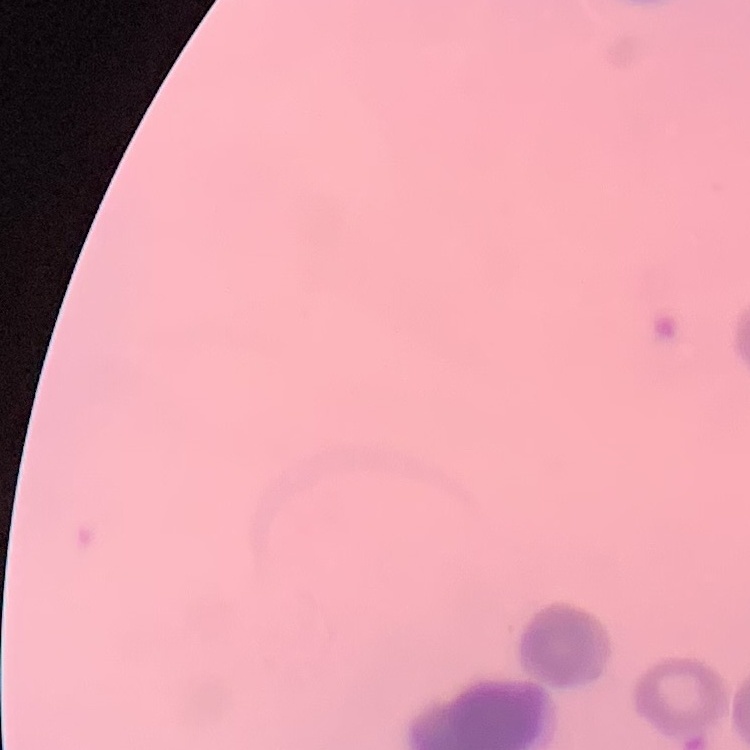

Summary:
  - Red blood cell morphology: rouleaux formation
  - Stain: Field's or Giemsa
  - Image type: square crop of a larger photomicrograph
  - Preparation: thin blood smear